Locate every blood parasite and identify its species.
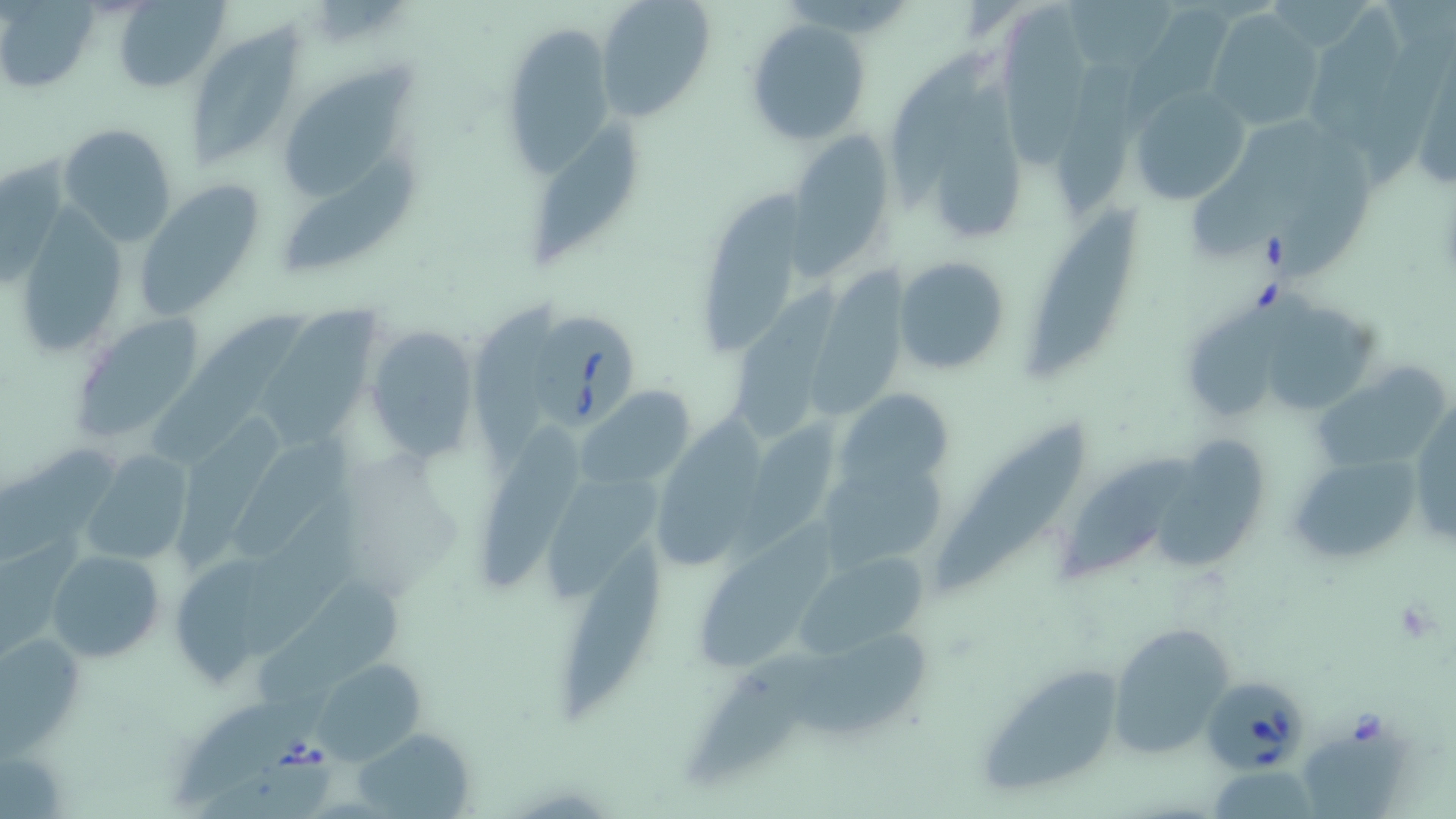
Approximate bounding boxes as (x1, y1, x2, y2) in pixels.
Babesia divergens-infected red blood cells: (524, 307, 638, 432), (1205, 676, 1304, 770).
No Plasmodium falciparum, Plasmodium ovale, Plasmodium malariae, Plasmodium vivax, or Trypanosoma brucei observed.

slide_level_diagnosis: Babesia divergens
platelet_locations: 'approximate bounding boxes as (x1, y1, x2, y2) in pixels: (1393, 599, 1439, 644)'
stain: May-Grünwald-Giemsa
preparation: thin blood film
modality: light microscopy
image_size: 1456×819 pixels
uninfected_red_blood_cell_locations: 'approximate bounding boxes as (x1, y1, x2, y2) in pixels: (595, 0, 715, 121), (1068, 0, 1174, 75), (112, 1, 228, 91), (996, 1, 1097, 164), (1, 4, 98, 93), (1205, 9, 1323, 131), (1312, 10, 1403, 149), (747, 18, 872, 147), (505, 21, 615, 186), (191, 22, 302, 170), (888, 45, 996, 217), (1057, 45, 1159, 214), (293, 61, 422, 200), (1409, 61, 1456, 197), (932, 76, 1031, 237), (1129, 85, 1250, 208), (524, 117, 648, 266), (58, 123, 180, 246), (1194, 123, 1322, 259), (787, 130, 898, 270), (1274, 132, 1375, 279), (284, 146, 417, 271), (1, 153, 66, 283), (134, 183, 265, 318), (704, 188, 804, 355), (1030, 208, 1139, 372), (893, 256, 1012, 375), (811, 272, 911, 417), (732, 288, 843, 439), (1188, 293, 1309, 418), (266, 298, 378, 451), (160, 300, 300, 464), (1275, 302, 1381, 413), (71, 316, 203, 443), (366, 326, 479, 463), (1310, 363, 1449, 465), (579, 386, 697, 488), (837, 387, 955, 496), (181, 400, 283, 567), (484, 411, 590, 593), (657, 412, 766, 570), (736, 412, 838, 559), (234, 414, 352, 566), (935, 422, 1085, 595), (1161, 430, 1271, 568), (8, 441, 133, 567), (81, 449, 193, 568), (1289, 451, 1425, 564), (1064, 455, 1194, 580), (821, 458, 943, 569), (550, 473, 664, 597), (239, 502, 371, 659), (697, 516, 840, 676), (563, 536, 662, 718), (45, 547, 166, 663), (795, 550, 927, 657), (172, 552, 269, 687), (256, 577, 415, 711), (1106, 620, 1239, 757), (1, 629, 84, 746), (789, 633, 938, 731), (694, 643, 834, 781), (311, 658, 426, 763), (969, 659, 1133, 801), (172, 680, 332, 804), (355, 728, 476, 818), (1303, 733, 1403, 819), (1218, 766, 1312, 819)'
magnification: 1000x
field_of_view: one of a larger specimen